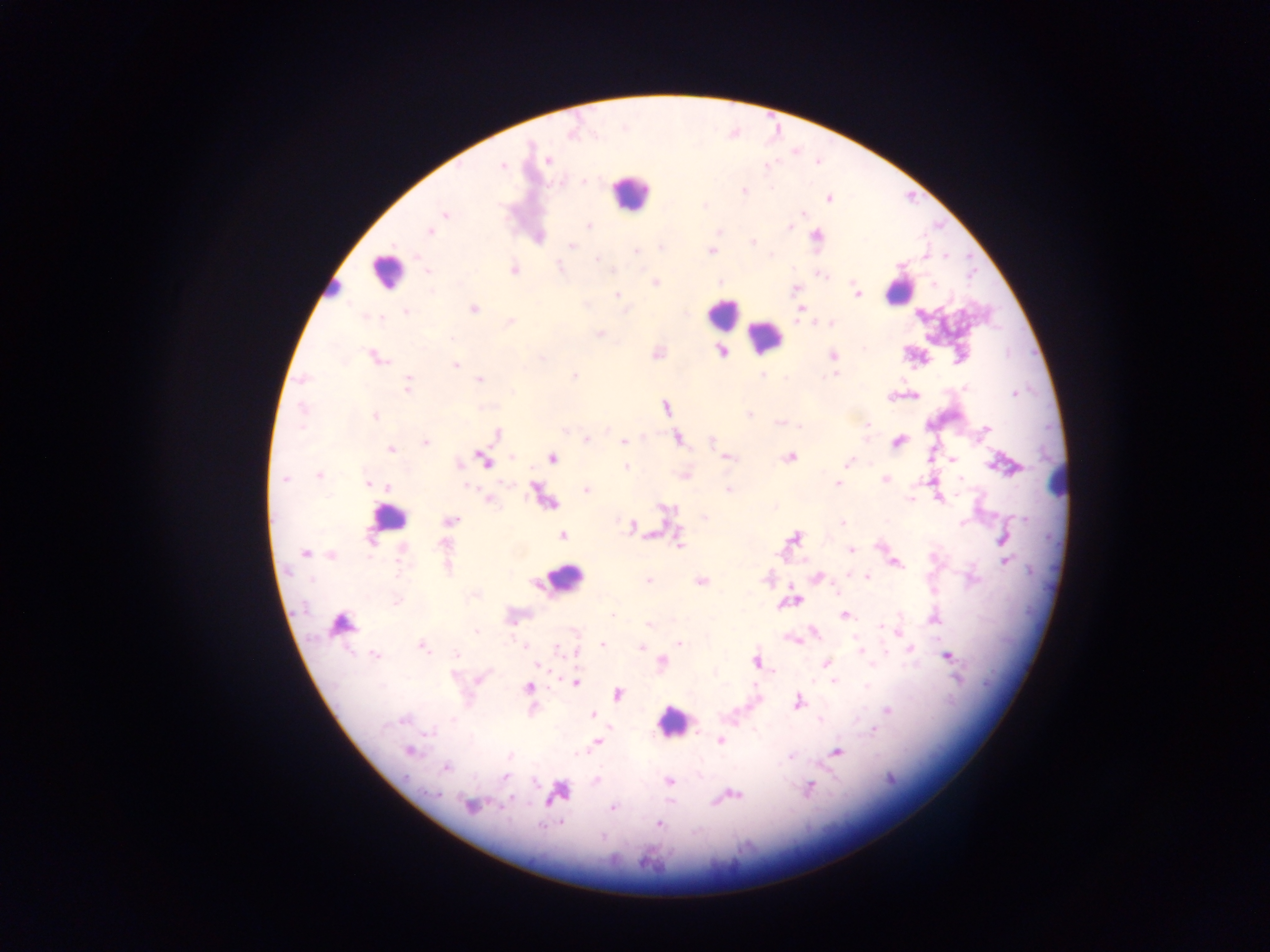
country = Ghana
field of view = single
image size = 1270×952 pixels
leukocyte locations = approximate centers as (x, y) in pixels (subset; some below the resolvable size): (629, 192), (386, 271), (331, 289), (898, 289), (722, 313), (765, 336), (1057, 482), (388, 517), (563, 580), (339, 629), (673, 720)
preparation = thick blood film
Plasmodium parasite locations = approximate centers as (x, y) in pixels: (548, 159), (502, 166), (584, 181), (745, 190), (828, 198), (445, 214), (803, 214), (589, 226), (789, 227), (429, 231), (815, 235), (752, 242), (572, 246), (661, 247), (636, 251), (710, 252), (945, 255), (597, 259), (559, 267), (513, 270), (613, 270), (427, 271), (719, 282), (654, 283), (933, 284), (795, 289), (618, 294), (858, 294), (473, 309), (407, 310), (510, 322), (830, 324), (599, 333), (721, 352), (833, 355), (377, 358), (542, 358), (455, 365), (762, 374), (836, 374), (571, 376), (825, 378), (479, 380), (408, 385), (966, 388), (1014, 394), (665, 407), (302, 408), (748, 415), (375, 416), (778, 423), (866, 425), (801, 427), (987, 428), (496, 434), (677, 439), (586, 440), (711, 441), (623, 442), (426, 443), (391, 449), (512, 457), (727, 457), (790, 457), (553, 458), (953, 459), (485, 461), (848, 462), (626, 467), (319, 475), (685, 475), (285, 479), (885, 479), (961, 479), (367, 484), (837, 484), (467, 486), (387, 487), (728, 489), (586, 490), (490, 500), (704, 517), (450, 521), (842, 523), (962, 523), (631, 527), (562, 536), (795, 538), (370, 540), (680, 544), (851, 550), (305, 553), (331, 555), (1005, 561), (896, 563), (447, 568), (817, 576), (867, 576), (648, 579), (311, 580), (701, 581), (834, 589), (796, 601), (396, 602), (613, 616), (846, 616), (649, 625), (881, 626), (477, 632), (679, 643), (602, 644), (640, 646), (423, 647), (910, 649), (861, 651), (457, 654), (375, 655), (947, 657), (756, 660), (662, 661), (826, 664), (536, 666), (453, 675), (480, 678), (834, 681), (575, 682), (529, 688), (617, 694), (798, 702), (887, 710), (593, 714), (403, 720), (874, 730), (431, 732), (720, 740), (598, 741), (409, 751), (837, 751), (446, 767), (505, 777), (596, 781), (669, 781), (809, 788), (557, 793), (435, 794), (731, 795), (470, 805), (612, 808), (659, 824)
capture = mobile-phone photograph through a microscope